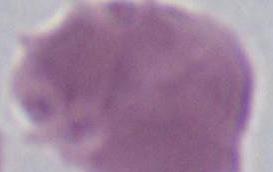

Summary:
  - Modality: photomicrograph
  - Identification: red blood cell
  - Magnification: 1000x